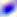

{
  "modality": "micrograph",
  "magnification": "400x",
  "identification": "Toxoplasma gondii"
}